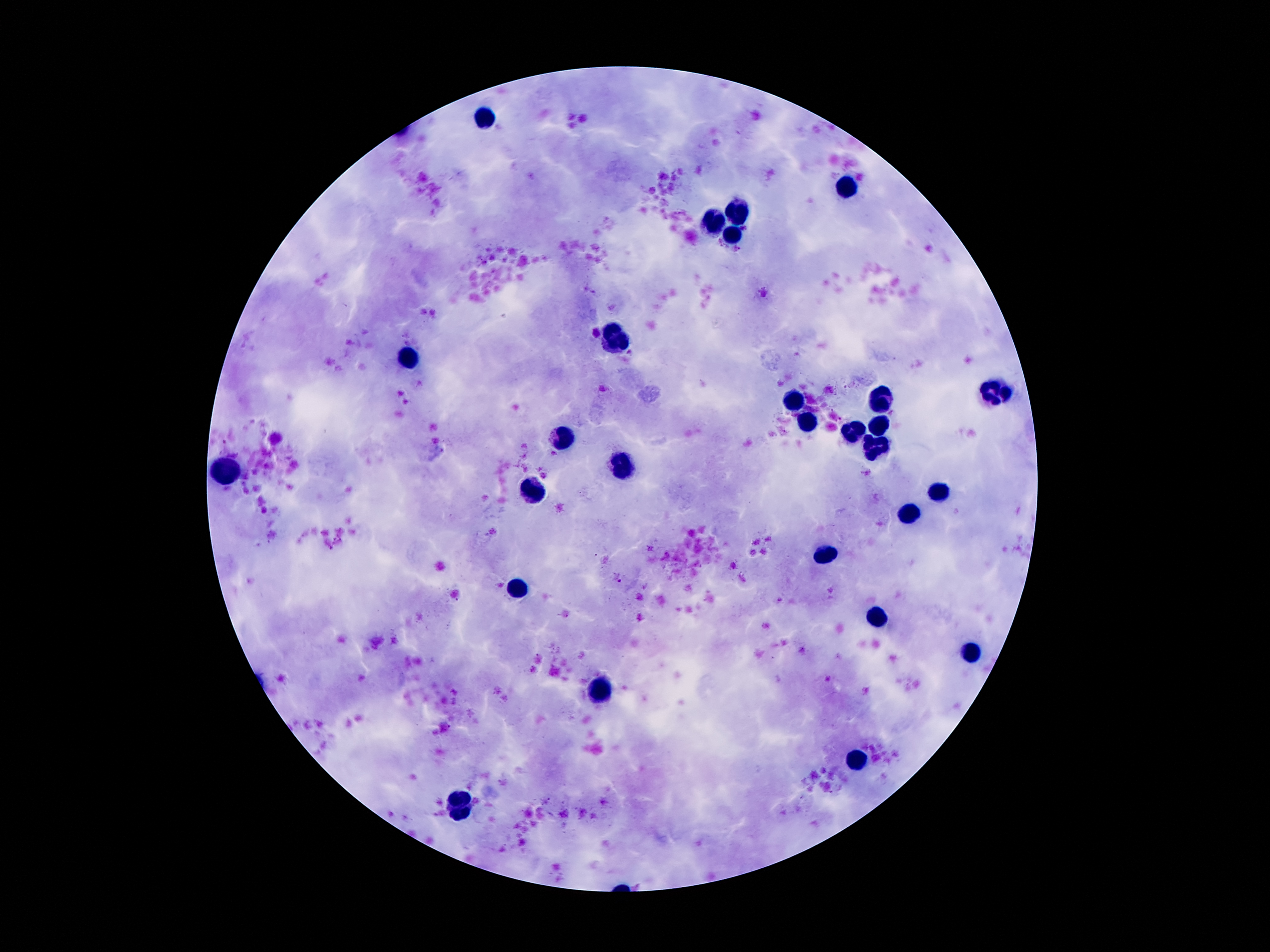
{
  "magnification": "100x",
  "malaria_parasite_locations": "approximate object centers, in pixels from the top-left corner: (x=617, y=577)",
  "capture": "smartphone through the microscope eyepiece",
  "image_size": "1270×952 pixels",
  "leukocyte_locations": "approximate object centers, in pixels from the top-left corner: (x=486, y=118), (x=847, y=188), (x=740, y=212), (x=717, y=223), (x=731, y=233), (x=615, y=339), (x=409, y=358), (x=997, y=391), (x=881, y=400), (x=797, y=401), (x=808, y=423), (x=879, y=426), (x=854, y=432), (x=563, y=438), (x=874, y=448), (x=625, y=466), (x=225, y=473), (x=531, y=491), (x=936, y=491), (x=906, y=513), (x=822, y=557), (x=520, y=587), (x=879, y=621), (x=972, y=652), (x=597, y=691), (x=856, y=759), (x=457, y=802)",
  "stain": "Giemsa",
  "field_of_view": "one from this slide",
  "patient_malaria_status": "positive for Plasmodium falciparum",
  "preparation": "thick blood film"
}